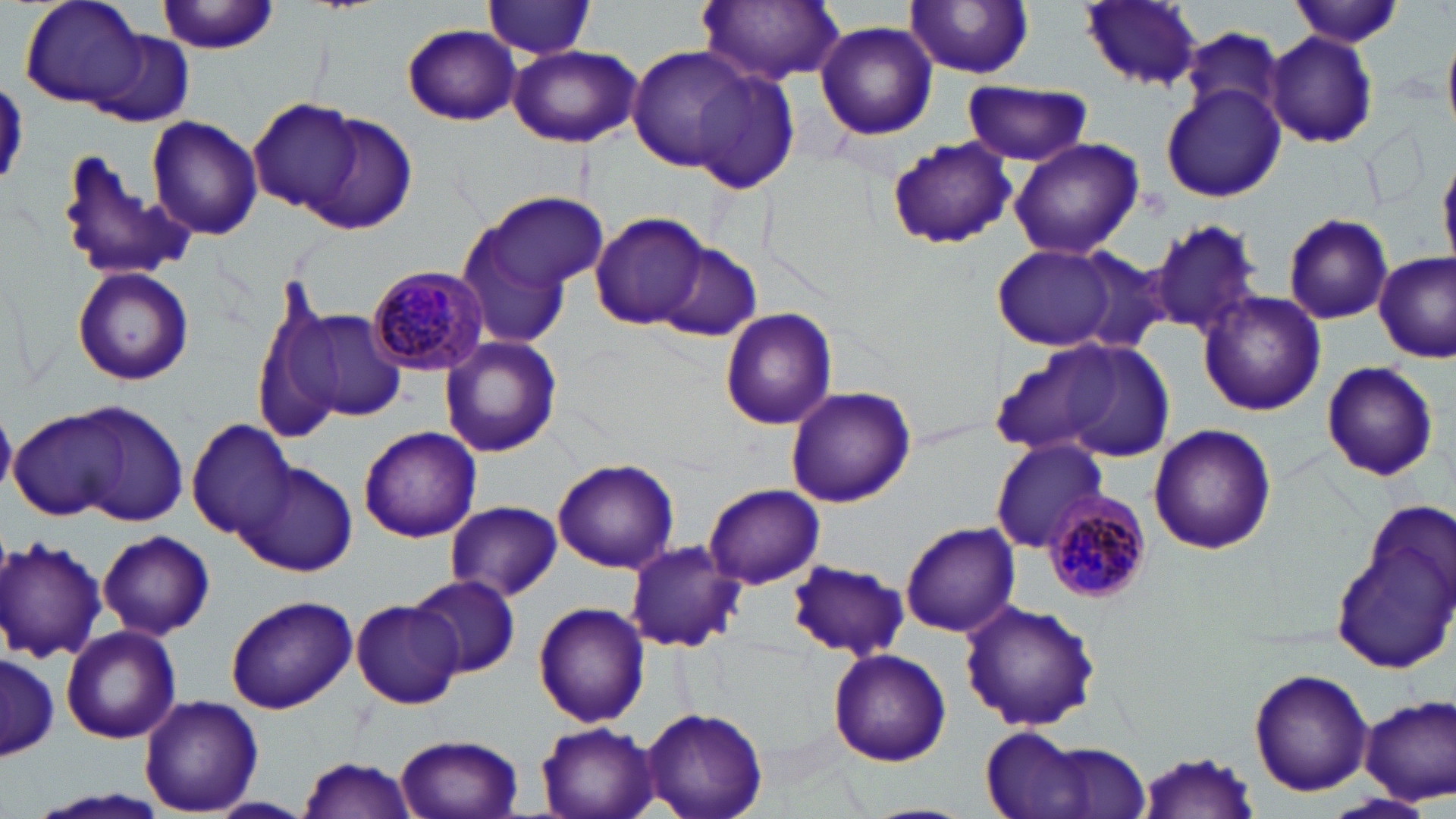
slide-level diagnosis = Plasmodium malariae
image size = 1456×819 pixels
uninfected red blood cell locations = approximate bounding boxes as (x1,y1)-(x2,y2) corner pairs in pixels: (22,0)-(148,107), (157,0)-(283,56), (485,0)-(595,57), (1288,0)-(1405,47), (694,1)-(848,84), (908,1)-(1033,77), (1079,1)-(1205,90), (815,22)-(938,140), (403,24)-(522,124), (1184,26)-(1286,126), (1265,31)-(1379,149), (90,34)-(192,126), (1444,38)-(1456,132), (509,44)-(640,147), (626,46)-(766,176), (687,69)-(800,192), (962,82)-(1095,166), (1160,84)-(1286,204), (249,100)-(364,217), (147,115)-(265,241), (308,115)-(417,233), (886,136)-(1017,249), (1008,138)-(1143,261), (55,150)-(194,284), (463,190)-(608,326), (590,211)-(710,330), (1282,212)-(1394,325), (1148,219)-(1265,337), (657,243)-(761,340), (992,243)-(1126,352), (1067,250)-(1176,356), (1374,253)-(1455,362), (72,266)-(195,386), (251,270)-(341,450), (1198,290)-(1326,416), (718,307)-(839,431), (289,308)-(407,422), (996,334)-(1175,462), (440,336)-(562,458), (1319,359)-(1440,481), (787,387)-(915,508), (51,400)-(193,527), (10,410)-(129,521), (188,418)-(296,538), (1148,424)-(1276,555), (358,425)-(481,541), (989,438)-(1108,551), (553,460)-(679,574), (241,463)-(357,577), (704,482)-(825,588), (445,500)-(562,601), (1328,500)-(1455,675), (900,522)-(1019,638), (98,530)-(214,641), (0,537)-(107,661), (625,540)-(744,653), (786,559)-(909,660), (410,576)-(521,677), (225,594)-(357,714), (351,596)-(465,708), (959,599)-(1101,732), (533,602)-(650,728), (59,625)-(181,744), (827,647)-(951,765), (1,649)-(58,762), (1248,669)-(1373,797), (1359,695)-(1456,805), (139,696)-(263,814), (642,707)-(768,818), (535,720)-(662,819), (981,731)-(1145,819), (394,733)-(525,819), (1138,750)-(1260,819), (296,755)-(419,819), (1325,794)-(1437,819), (208,798)-(313,818), (863,804)-(973,819)
preparation = thin blood smear
modality = light microscopy
field of view = one of a larger specimen
magnification = 1000x
stain = May-Grünwald-Giemsa
Plasmodium malariae-infected red blood cell locations = approximate bounding boxes as (x1,y1)-(x2,y2) corner pairs in pixels: (365,264)-(490,377), (1044,492)-(1153,605)